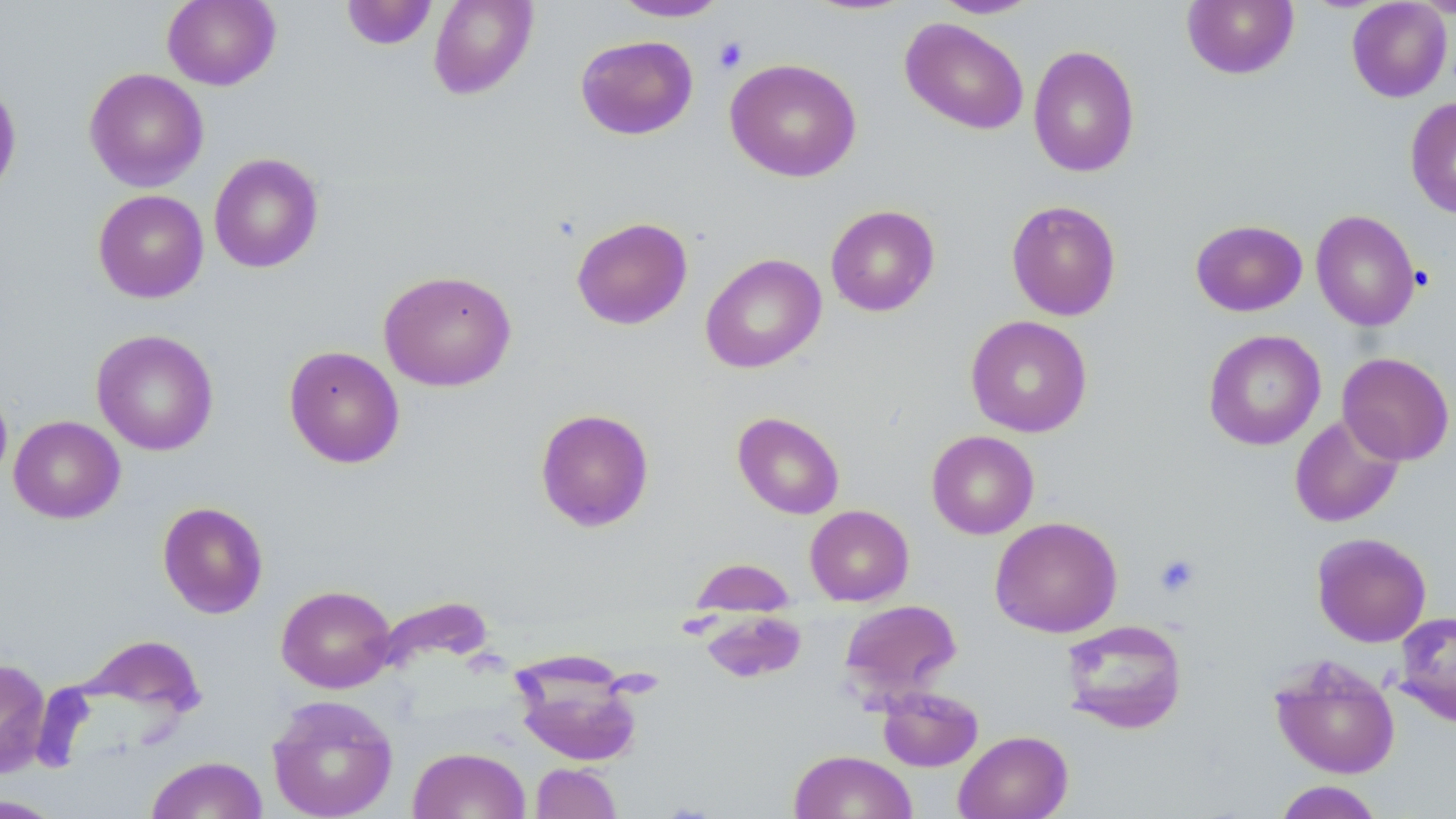

Approximate bounding boxes as [x1, y1, x2, y2] in pixels. Platelet locations: [713, 37, 749, 74], [1153, 552, 1201, 598]. Uninfected red blood cell locations: [162, 0, 281, 90], [428, 0, 538, 100], [932, 0, 1042, 19], [1182, 0, 1300, 80], [341, 1, 438, 51], [611, 1, 731, 22], [1346, 1, 1452, 102], [900, 17, 1029, 135], [575, 35, 698, 140], [1028, 45, 1140, 177], [725, 58, 862, 182], [84, 68, 209, 191], [0, 77, 22, 201], [1405, 97, 1456, 219], [208, 153, 324, 274], [92, 189, 208, 303], [1006, 199, 1122, 321], [825, 204, 940, 317], [1311, 210, 1421, 332], [571, 216, 693, 330], [1190, 219, 1307, 316], [700, 253, 826, 373], [378, 269, 517, 391], [965, 315, 1093, 437], [91, 329, 219, 455], [1203, 329, 1326, 451], [283, 345, 405, 469], [1337, 351, 1455, 466], [0, 384, 12, 490], [535, 408, 655, 532], [732, 412, 845, 519], [1289, 413, 1405, 528], [9, 416, 125, 524], [926, 431, 1039, 539], [157, 501, 268, 619], [805, 505, 914, 606], [990, 516, 1122, 638], [1311, 532, 1432, 647], [690, 557, 796, 615], [276, 585, 396, 693], [839, 598, 962, 702], [702, 611, 807, 683], [1394, 611, 1456, 727], [1060, 619, 1187, 735], [512, 654, 646, 767], [1269, 655, 1401, 779], [0, 658, 50, 778], [876, 685, 984, 772], [267, 694, 398, 819], [953, 730, 1073, 819], [407, 746, 530, 819], [788, 750, 918, 819], [145, 755, 268, 818], [530, 762, 622, 819], [1272, 780, 1385, 819], [0, 794, 67, 818]. Slide-level diagnosis: no evidence of blood parasites. Image is 1456×819 pixels. Optical microscopy. One field of a larger specimen. Captured at 1000x magnification. Thin blood film. May-Grünwald-Giemsa-stained preparation.